Assess this cell for malaria.
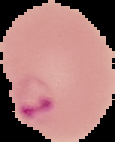

It is parasitized.

From a thin blood smear. Image is 115×142 pixels. Cell region segmented out of the field of view; the surrounding area is masked to black.